Assess this cell for malaria.
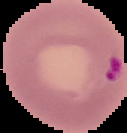

It is parasitized.

preparation = thin blood film
image type = segmented cell region on a black background
image size = 127×133 pixels